Name the parasite shown.
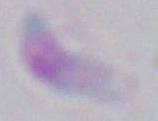
This is Toxoplasma gondii.

1000x magnification. Micrograph.